Identify the parasite.
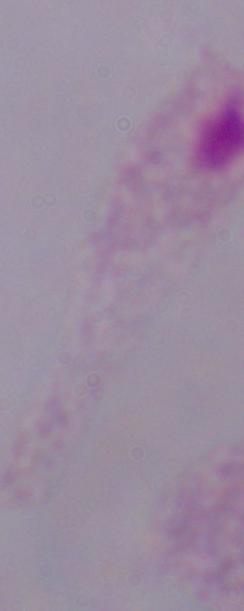

A trichomonad.

modality = micrograph
magnification = 1000x